Outline each blood parasite and name the species.
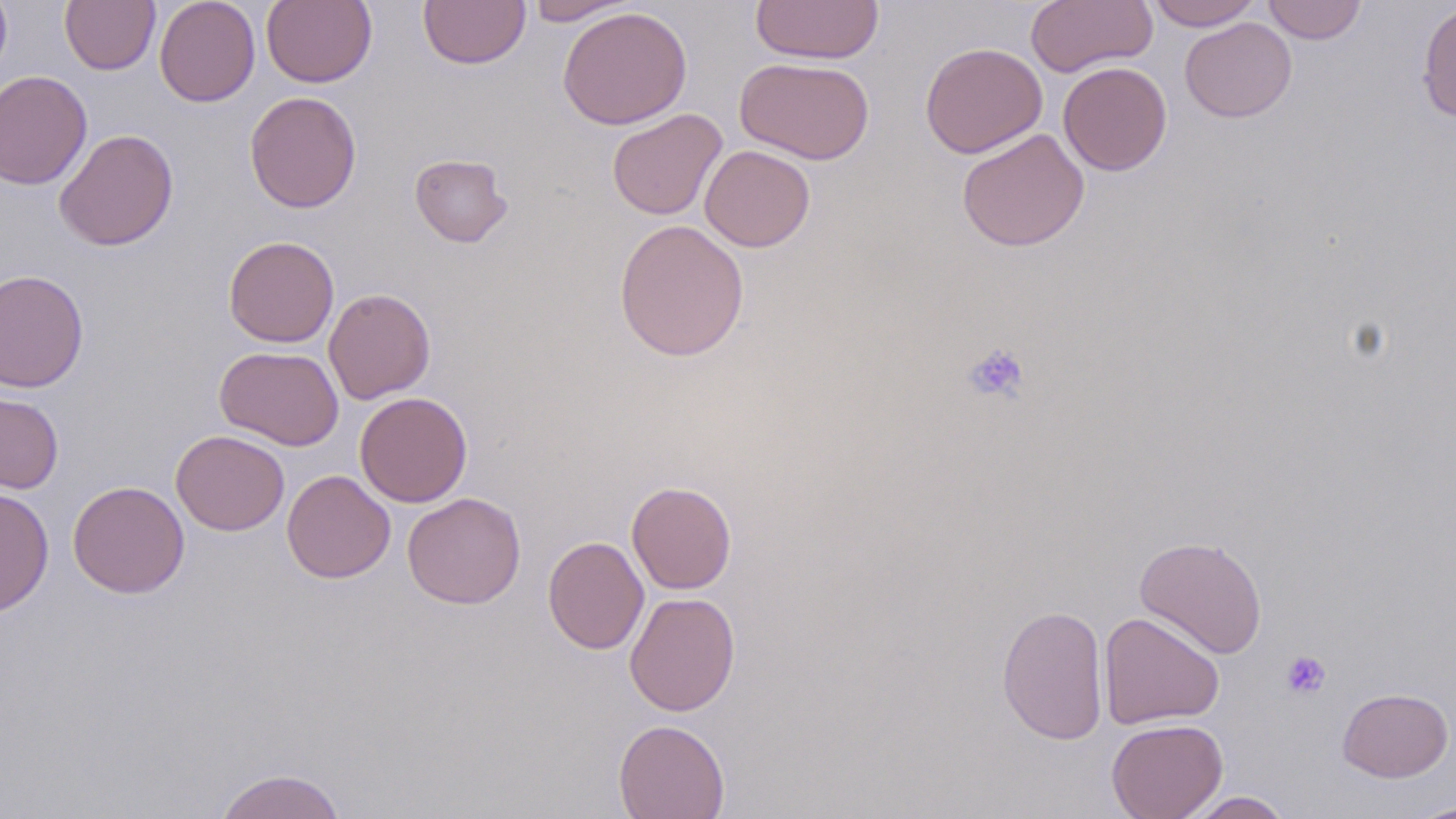

No blood parasites seen.

Approximate bounding boxes as (x1,y1)-(x2,y2) corner pairs in pixels. Uninfected red blood cell locations: (0,0)-(12,82), (60,0)-(160,74), (154,0)-(260,107), (261,0)-(377,88), (419,0)-(530,69), (523,0)-(639,26), (751,0)-(884,65), (1025,0)-(1157,77), (1146,0)-(1262,30), (1262,0)-(1366,44), (1417,1)-(1456,123), (557,6)-(692,130), (1180,17)-(1297,122), (920,42)-(1047,158), (735,56)-(874,165), (1058,61)-(1172,175), (0,69)-(92,190), (245,91)-(362,213), (606,108)-(728,221), (54,128)-(179,251), (957,128)-(1090,252), (700,145)-(815,252), (410,153)-(513,247), (613,219)-(750,362), (223,235)-(339,348), (0,268)-(89,393), (323,287)-(436,405), (215,345)-(344,451), (0,391)-(64,494), (355,392)-(472,507), (171,430)-(289,536), (282,469)-(395,583), (67,480)-(190,598), (626,480)-(737,594), (0,487)-(54,616), (402,492)-(526,609), (1133,535)-(1268,659), (543,536)-(648,654), (625,591)-(740,717), (996,604)-(1109,745), (1098,611)-(1225,730), (1337,687)-(1453,782), (1106,718)-(1228,819), (613,719)-(730,818), (213,768)-(347,819), (1180,791)-(1294,818), (1406,801)-(1455,819). Platelet locations: (962,342)-(1030,404), (1280,649)-(1331,699). Slide-level diagnosis: no evidence of blood parasites. Thin blood film. One field of a larger specimen. Image is 1456×819 pixels. Optical microscopy. Captured at 1000x magnification. May-Grünwald-Giemsa-stained preparation.